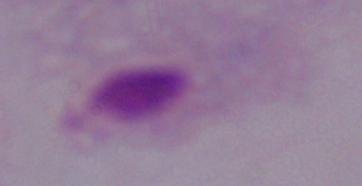
Summary:
  - Magnification: 1000x
  - Modality: micrograph
  - Identification: trichomonad